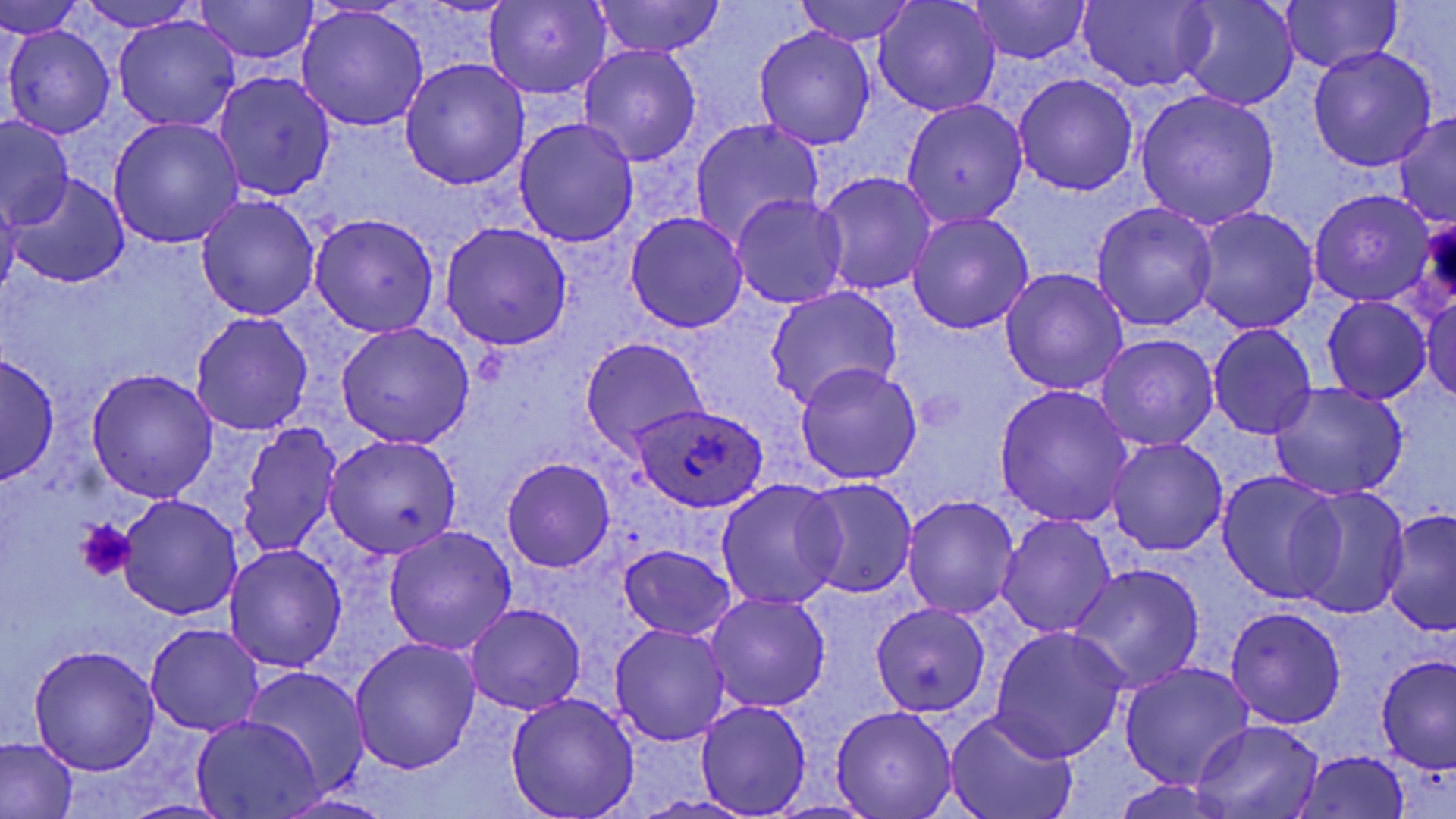
slide_level_diagnosis: Plasmodium ovale
field_of_view: single
stain: May-Grünwald-Giemsa
platelet_locations: 'approximate bounding boxes as [x1, y1, x2, y2] in pixels: [76, 517, 132, 579]'
plasmodium_ovale_infected_red_blood_cell_locations: 'approximate bounding boxes as [x1, y1, x2, y2] in pixels: [632, 402, 768, 512]'
modality: light microscopy
uninfected_red_blood_cell_locations: 'approximate bounding boxes as [x1, y1, x2, y2] in pixels: [0, 0, 88, 41], [73, 0, 206, 32], [793, 0, 918, 46], [968, 0, 1091, 64], [1174, 0, 1299, 111], [195, 1, 318, 64], [484, 1, 611, 100], [590, 1, 724, 57], [874, 1, 1000, 117], [1280, 1, 1403, 74], [1074, 2, 1215, 90], [297, 9, 429, 131], [112, 14, 240, 130], [6, 25, 116, 140], [754, 26, 875, 150], [579, 45, 701, 166], [1307, 46, 1438, 171], [400, 58, 530, 190], [215, 71, 335, 201], [1014, 73, 1139, 195], [1135, 89, 1281, 230], [901, 99, 1028, 227], [1392, 111, 1455, 226], [515, 117, 640, 247], [1, 118, 75, 230], [108, 118, 243, 249], [689, 119, 823, 247], [5, 172, 128, 289], [816, 172, 937, 296], [1308, 189, 1436, 306], [0, 194, 22, 300], [197, 194, 320, 321], [730, 194, 849, 308], [1092, 202, 1218, 331], [1191, 207, 1319, 333], [624, 212, 748, 332], [907, 212, 1034, 334], [309, 213, 440, 337], [440, 221, 572, 350], [1000, 268, 1129, 396], [765, 285, 903, 410], [1321, 295, 1432, 404], [1423, 295, 1456, 402], [191, 312, 313, 436], [335, 323, 473, 447], [1207, 324, 1317, 439], [1095, 333, 1218, 451], [580, 336, 708, 454], [1218, 342, 1383, 479], [0, 351, 59, 486], [795, 362, 923, 485], [87, 370, 219, 503], [1269, 381, 1408, 502], [995, 384, 1134, 528], [237, 421, 344, 559], [324, 434, 461, 558], [1107, 437, 1227, 555], [502, 457, 615, 572], [1217, 471, 1347, 605], [798, 477, 919, 599], [717, 479, 846, 609], [1289, 487, 1409, 620], [118, 494, 241, 621], [902, 494, 1020, 620], [1382, 509, 1456, 634], [997, 515, 1117, 636], [383, 526, 518, 655], [225, 544, 347, 673], [619, 545, 736, 639], [1068, 563, 1206, 692], [704, 592, 830, 713], [870, 602, 990, 716], [465, 603, 584, 714], [1226, 606, 1346, 729], [145, 622, 266, 736], [609, 623, 733, 746], [989, 627, 1129, 762], [350, 638, 481, 775], [30, 645, 160, 773], [1376, 653, 1455, 775], [1118, 660, 1255, 790], [244, 666, 370, 796], [504, 692, 639, 818], [696, 699, 811, 817], [831, 705, 958, 817], [944, 710, 1079, 819], [191, 715, 325, 819], [1191, 720, 1324, 817], [0, 737, 78, 819], [1292, 750, 1412, 819], [276, 794, 400, 818], [633, 794, 760, 818]'
magnification: 1000x
preparation: thin blood film
image_size: 1456×819 pixels